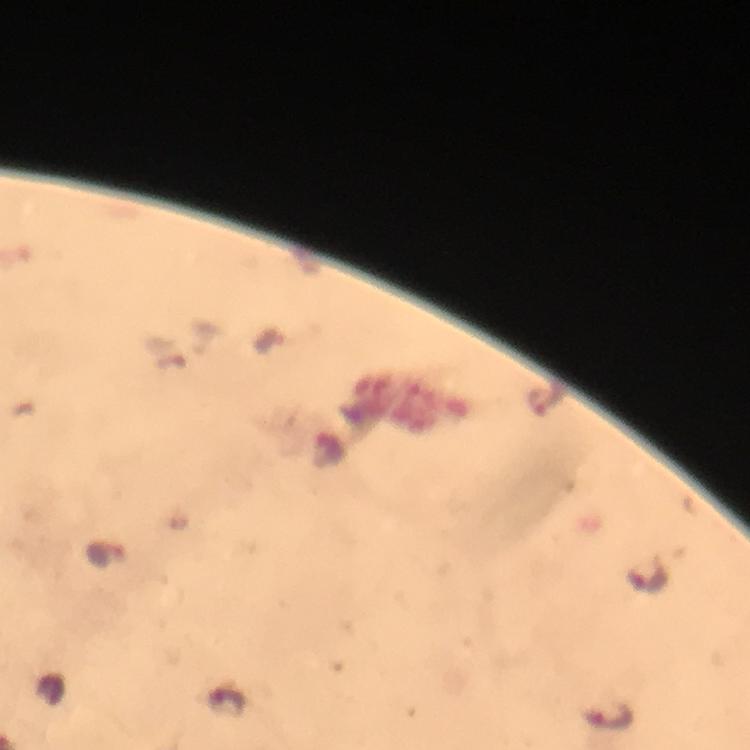 Approximate centers as [x, y] in pixels. Malaria parasite locations: [545, 397], [106, 554], [647, 578], [228, 701], [608, 717]. At 100x magnification. Giemsa stain. From a malaria diagnostic workup. Immersion oil was used. Photographed through the microscope with a smartphone camera. Image is 750×750 pixels. A crop from one field of view. Thick blood smear.